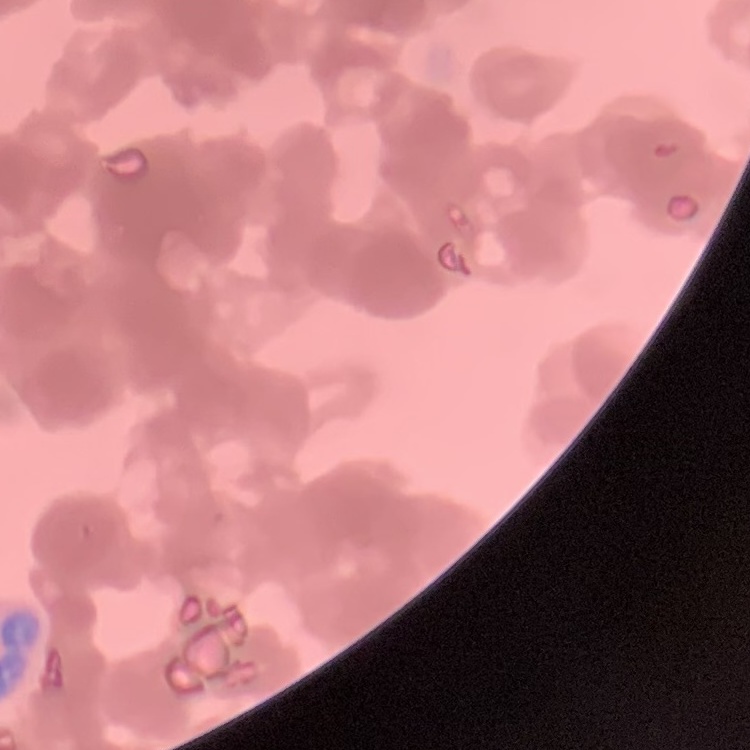 The erythrocytes show rouleaux formation. Square crop of a larger photomicrograph. Thin peripheral smear. Field's or Giemsa stain.